Identify the parasite.
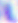

This is Toxoplasma gondii.

Micrograph. 400x magnification.